Give the preparation type.
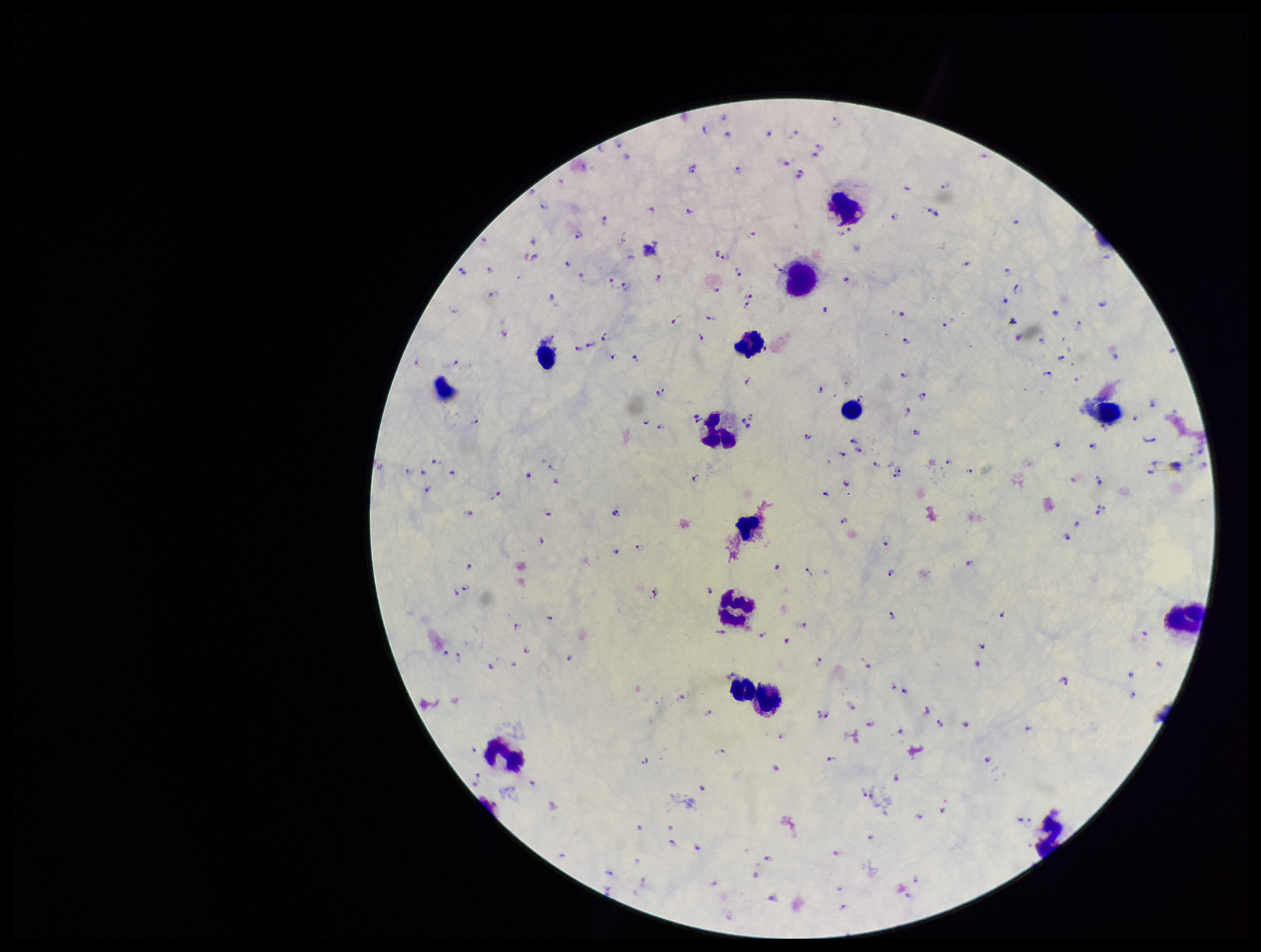

Thick.

Image is 1261×952 pixels. Parasite count: 208. Stained with Giemsa. Patient malaria status: infected. Smartphone photograph taken through the eyepiece of a microscope. One field from this slide. Species reported for this patient: Plasmodium falciparum. Plasmodium parasites: seen. Leukocyte count: 13.